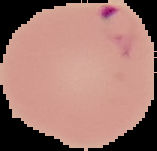

{
  "image_size": "157×151 pixels",
  "malaria_status": "parasitized",
  "image_type": "cell region segmented out of the field of view; surrounding area masked to black",
  "preparation": "thin blood film"
}